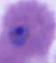

Summary:
  - Modality: photomicrograph
  - Identification: Plasmodium
  - Magnification: 400x or 1000x